Describe the morphology of the red blood cells.
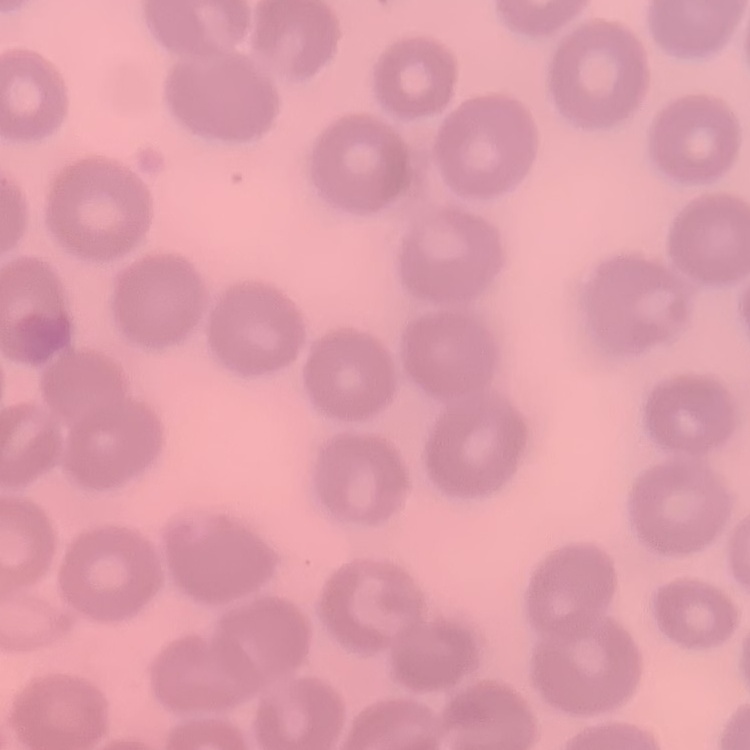
No rouleaux formation.

Thin blood film. One tile cut from a larger photomicrograph. Field's or Giemsa stain.